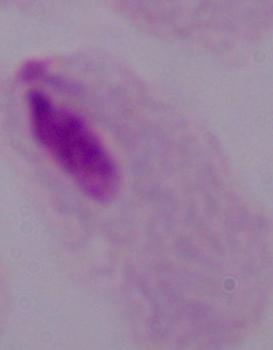
Summary:
  - Identification: trichomonad
  - Modality: micrograph
  - Magnification: 1000x